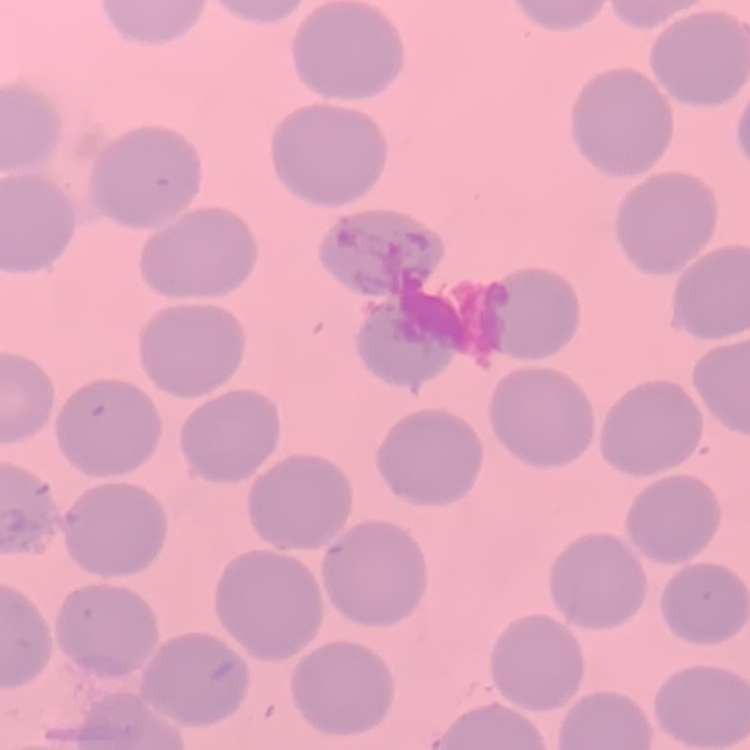
{
  "erythrocyte_morphology": "no rouleaux formation",
  "image_type": "one tile cut from a larger photomicrograph",
  "preparation": "thin blood film",
  "stain": "Field's or Giemsa"
}